Comment on the morphology of the erythrocytes.
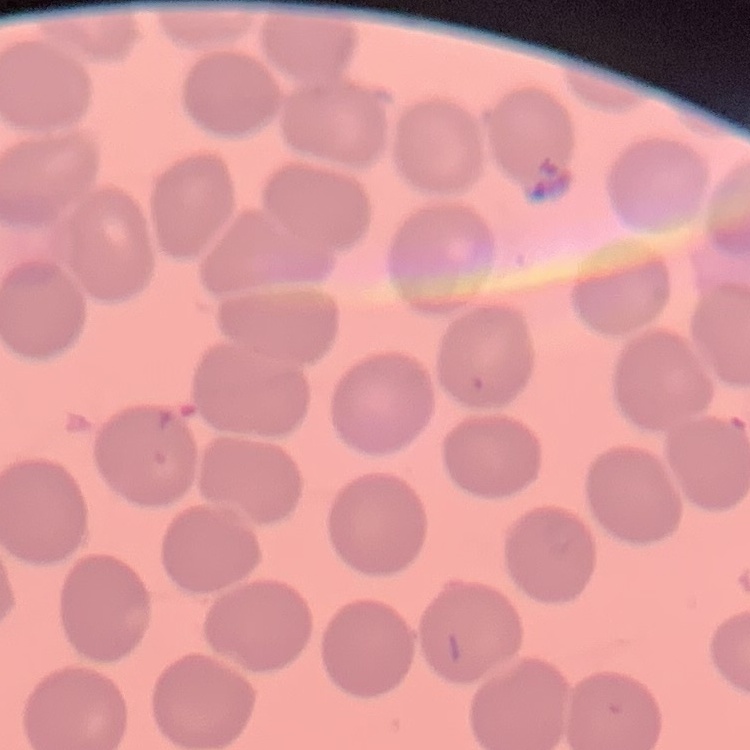

They show no rouleaux formation.

Summary:
  - Image type: one tile cut from a larger photomicrograph
  - Preparation: thin blood smear
  - Stain: Field's or Giemsa